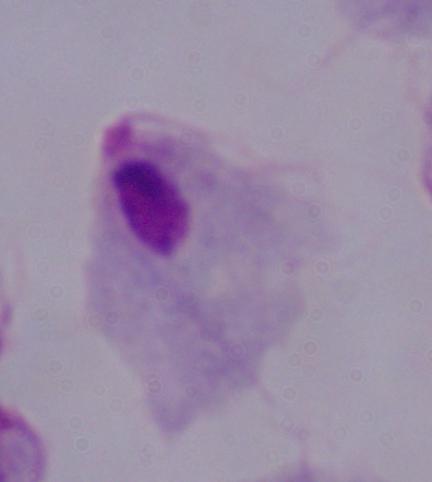

identification = trichomonad
magnification = 1000x
modality = photomicrograph